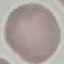

Summary:
  - Result: no malaria parasites seen
  - Preparation: thin blood film
  - Stain: Giemsa
  - Image type: automatically extracted cell patch, resized to 64 × 64 pixels
  - Capture: smartphone through the microscope eyepiece